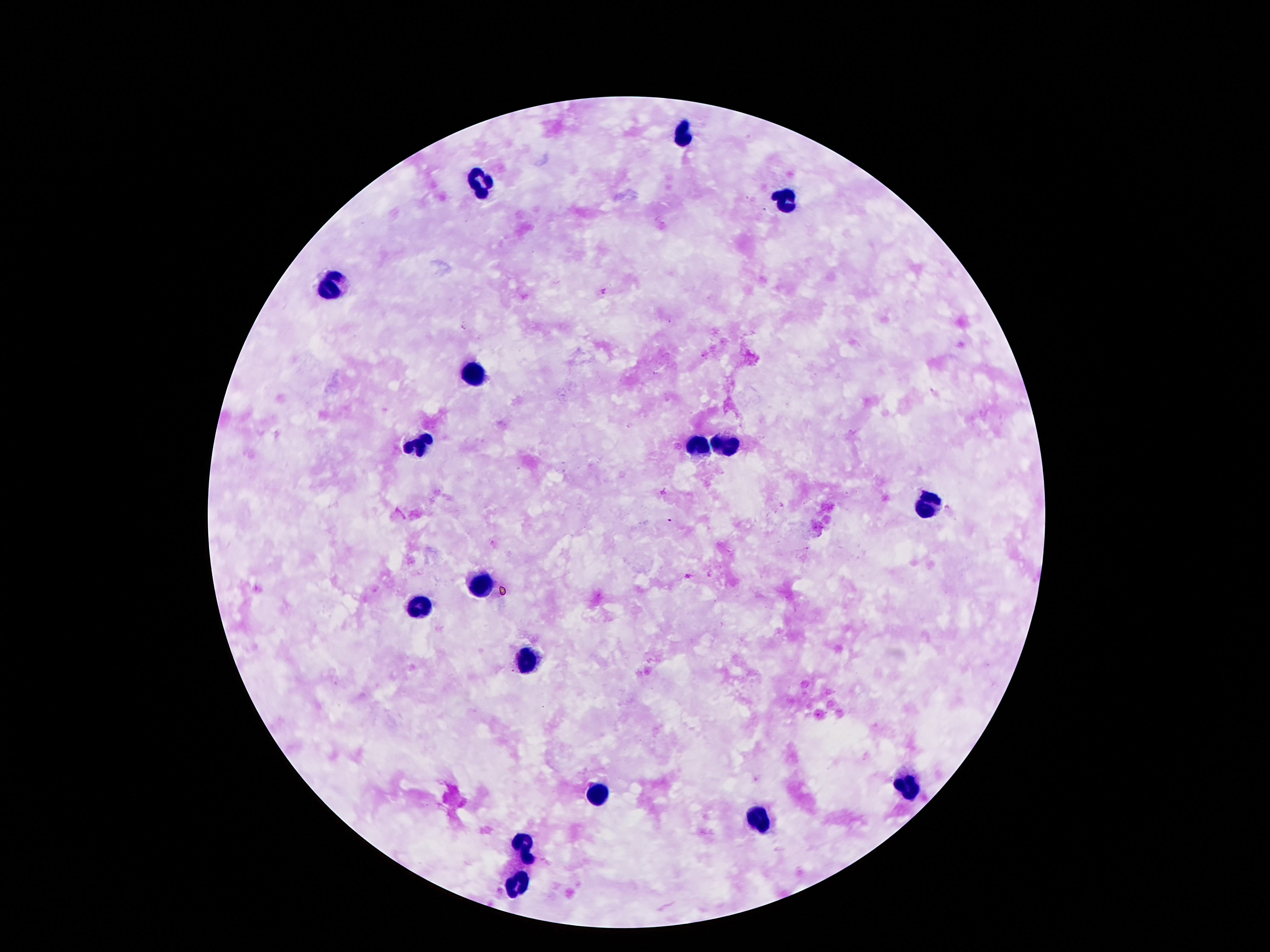 Approximate centers as {x, y} in pixels. Leukocyte locations: {682, 136}, {476, 183}, {782, 198}, {329, 289}, {472, 375}, {421, 440}, {694, 446}, {724, 448}, {923, 503}, {482, 583}, {421, 606}, {522, 662}, {904, 788}, {598, 795}, {759, 820}, {524, 845}, {514, 884}. Giemsa stain. Single field of view. Image is 1270×952 pixels. Patient malaria status: negative. Thick peripheral-blood smear. Smartphone photograph taken through the microscope eyepiece. 100x magnification.